Outline each uninfected red blood cell.
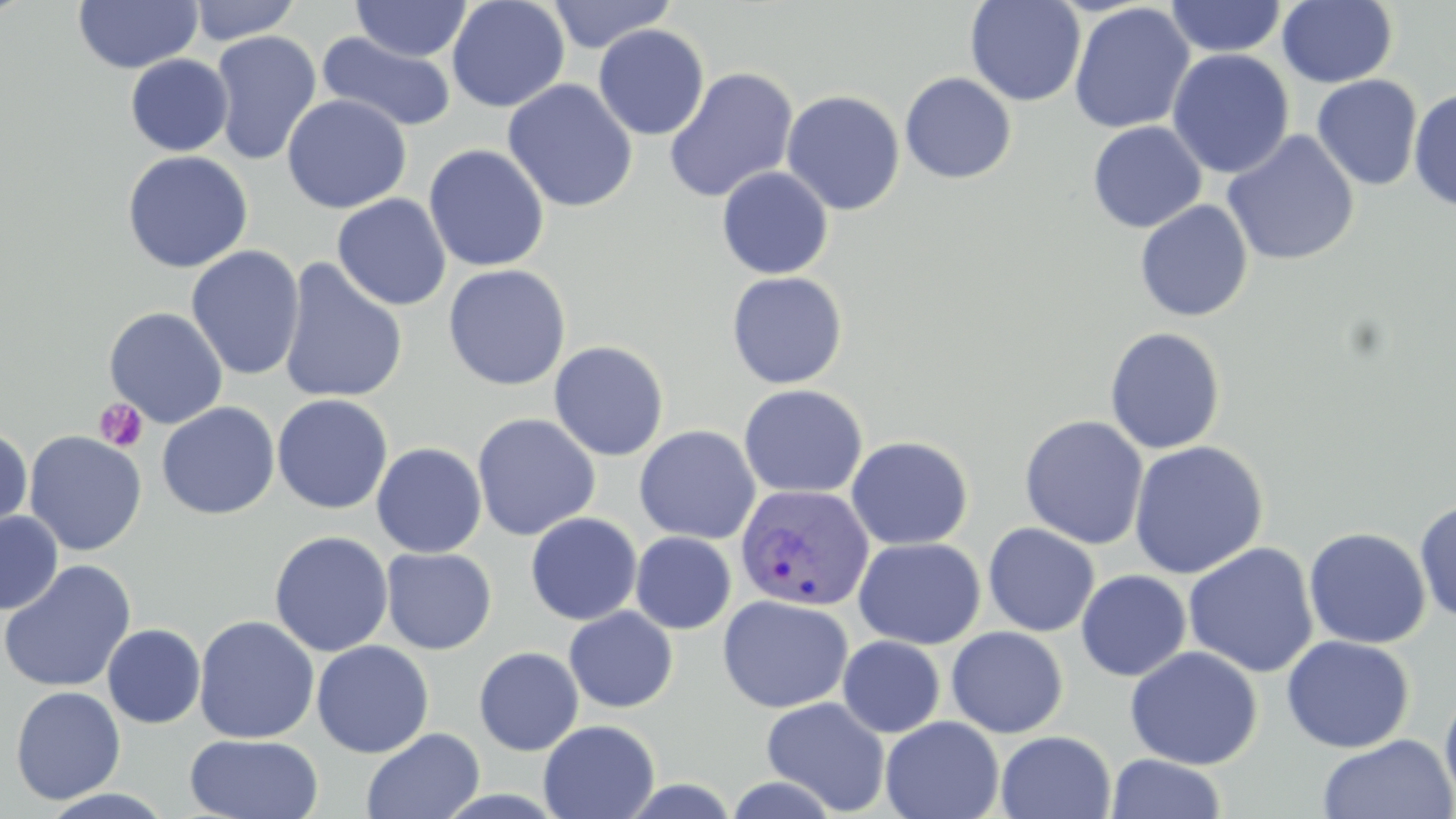

Approximate bounding boxes as (x1, y1, x2, y2) in pixels.
Uninfected red blood cells: (72, 0, 204, 74), (186, 0, 302, 44), (446, 0, 570, 113), (545, 0, 676, 53), (964, 0, 1086, 107), (351, 1, 472, 61), (1165, 1, 1287, 58), (1276, 1, 1398, 88), (1068, 3, 1194, 134), (593, 24, 710, 140), (210, 30, 322, 165), (317, 32, 457, 134), (1167, 49, 1295, 179), (125, 54, 233, 157), (663, 67, 799, 203), (899, 72, 1017, 184), (1312, 74, 1423, 191), (502, 79, 639, 213), (1408, 87, 1456, 213), (780, 90, 905, 216), (281, 94, 412, 214), (1087, 121, 1207, 233), (1221, 130, 1360, 266), (423, 144, 550, 272), (121, 150, 253, 273), (716, 166, 834, 280), (332, 193, 451, 311), (1134, 200, 1253, 322), (185, 246, 305, 382), (277, 258, 409, 404), (442, 263, 571, 391), (726, 271, 848, 389), (103, 306, 228, 428), (1104, 326, 1226, 455), (548, 340, 669, 461), (738, 383, 868, 499), (272, 394, 393, 514), (157, 401, 280, 520), (472, 413, 600, 541), (1019, 414, 1149, 549), (634, 425, 761, 544), (0, 426, 33, 539), (24, 431, 147, 556), (846, 435, 974, 551), (1129, 440, 1269, 579), (371, 442, 487, 558), (1414, 498, 1456, 623), (0, 510, 64, 615), (525, 512, 643, 626), (982, 522, 1100, 637), (1303, 527, 1431, 649), (269, 531, 393, 657), (630, 531, 737, 634), (853, 536, 985, 648), (1182, 542, 1319, 679), (381, 547, 497, 655), (0, 560, 137, 693), (1075, 569, 1192, 681), (717, 594, 854, 714), (564, 606, 679, 713), (193, 615, 320, 744), (102, 624, 206, 728), (946, 626, 1069, 738), (1282, 635, 1414, 753), (837, 636, 945, 737), (311, 640, 434, 758), (473, 646, 584, 756), (1124, 646, 1263, 771), (1439, 685, 1456, 812), (10, 686, 126, 805), (762, 696, 890, 815), (880, 716, 1004, 819), (538, 719, 660, 819), (361, 727, 485, 819), (995, 730, 1116, 819), (185, 734, 323, 819), (1317, 734, 1455, 819), (1106, 753, 1227, 818), (720, 773, 845, 818), (39, 788, 176, 819).

Platelet locations: (94, 398, 148, 452). Plasmodium vivax-infected red blood cell locations: (736, 482, 874, 612). Slide-level diagnosis: Plasmodium vivax. Optical microscopy. May-Grünwald-Giemsa-stained preparation. 1000x magnification. Thin blood film. One field of a larger specimen. Image is 1456×819 pixels.